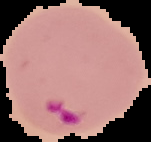

{
  "image_type": "segmented cell region with the area outside set to black",
  "result": "Plasmodium parasites detected",
  "image_size": "151×142 pixels",
  "preparation": "thin blood film"
}